Identify the blood parasite species.
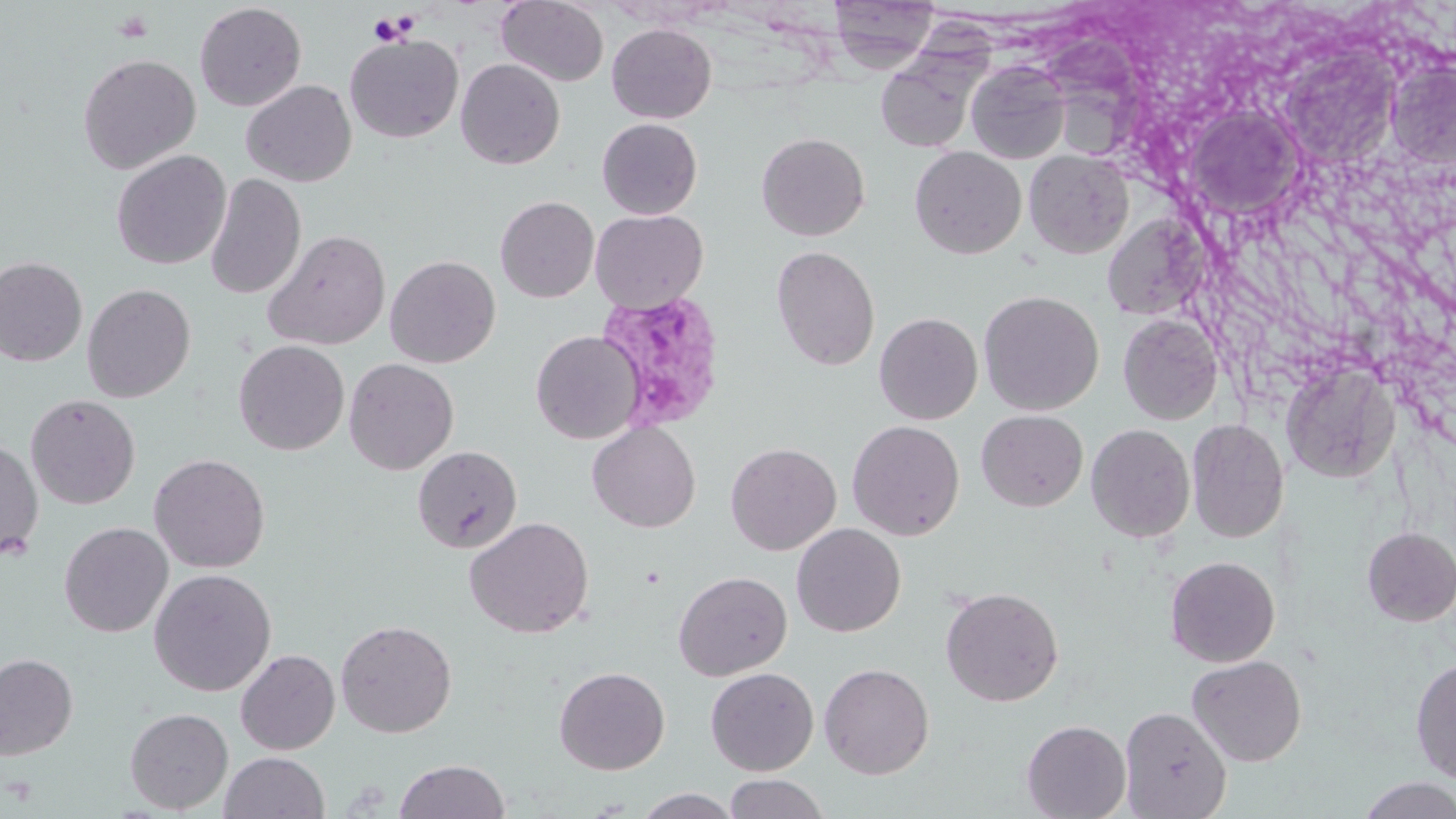

Plasmodium vivax.

Approximate bounding boxes as named x1/y1/x2/y2 corners in pixels. Platelet locations: (x1=368, y1=12, x2=415, y2=46). Plasmodium vivax-infected red blood cell locations: (x1=595, y1=288, x2=728, y2=434). Uninfected red blood cell locations: (x1=828, y1=0, x2=941, y2=71), (x1=496, y1=1, x2=609, y2=86), (x1=194, y1=2, x2=307, y2=112), (x1=606, y1=23, x2=717, y2=123), (x1=344, y1=33, x2=464, y2=143), (x1=1052, y1=33, x2=1145, y2=160), (x1=345, y1=45, x2=565, y2=157), (x1=77, y1=54, x2=201, y2=174), (x1=877, y1=56, x2=977, y2=153), (x1=455, y1=58, x2=566, y2=170), (x1=1386, y1=59, x2=1456, y2=170), (x1=966, y1=60, x2=1071, y2=165), (x1=241, y1=80, x2=356, y2=186), (x1=1186, y1=105, x2=1305, y2=220), (x1=597, y1=118, x2=702, y2=219), (x1=756, y1=132, x2=870, y2=241), (x1=910, y1=146, x2=1027, y2=258), (x1=1024, y1=149, x2=1134, y2=259), (x1=111, y1=150, x2=231, y2=269), (x1=205, y1=173, x2=306, y2=300), (x1=495, y1=196, x2=599, y2=302), (x1=1101, y1=204, x2=1213, y2=320), (x1=590, y1=209, x2=707, y2=313), (x1=263, y1=229, x2=391, y2=351), (x1=770, y1=245, x2=880, y2=371), (x1=385, y1=255, x2=500, y2=368), (x1=0, y1=256, x2=87, y2=366), (x1=82, y1=283, x2=196, y2=402), (x1=978, y1=290, x2=1104, y2=415), (x1=874, y1=312, x2=983, y2=425), (x1=1118, y1=313, x2=1222, y2=425), (x1=530, y1=330, x2=644, y2=444), (x1=233, y1=340, x2=349, y2=455), (x1=343, y1=357, x2=459, y2=475), (x1=1280, y1=361, x2=1399, y2=483), (x1=25, y1=394, x2=140, y2=509), (x1=976, y1=409, x2=1088, y2=511), (x1=1186, y1=418, x2=1289, y2=543), (x1=846, y1=420, x2=965, y2=541), (x1=587, y1=421, x2=701, y2=533), (x1=1086, y1=424, x2=1195, y2=542), (x1=0, y1=440, x2=44, y2=559), (x1=725, y1=442, x2=841, y2=555), (x1=412, y1=445, x2=522, y2=553), (x1=149, y1=453, x2=271, y2=573), (x1=464, y1=516, x2=594, y2=638), (x1=58, y1=521, x2=174, y2=637), (x1=791, y1=523, x2=906, y2=637), (x1=1361, y1=527, x2=1456, y2=626), (x1=1165, y1=555, x2=1281, y2=667), (x1=149, y1=568, x2=277, y2=696), (x1=673, y1=571, x2=792, y2=681), (x1=687, y1=571, x2=805, y2=778), (x1=940, y1=587, x2=1064, y2=707), (x1=335, y1=619, x2=457, y2=738), (x1=236, y1=649, x2=340, y2=754), (x1=0, y1=653, x2=78, y2=760), (x1=1186, y1=655, x2=1307, y2=766), (x1=1410, y1=657, x2=1456, y2=782), (x1=819, y1=662, x2=935, y2=779), (x1=554, y1=666, x2=670, y2=775), (x1=705, y1=667, x2=819, y2=776), (x1=1120, y1=706, x2=1232, y2=818), (x1=124, y1=707, x2=233, y2=814), (x1=1021, y1=719, x2=1131, y2=819), (x1=220, y1=751, x2=329, y2=818), (x1=393, y1=759, x2=510, y2=819), (x1=723, y1=774, x2=830, y2=819), (x1=1356, y1=776, x2=1456, y2=819), (x1=633, y1=788, x2=743, y2=818). Image is 1456×819 pixels. 1000x magnification. Single field of view. Optical microscopy. May-Grünwald-Giemsa stain. Thin blood film.